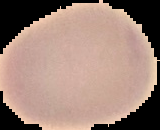

malaria status = uninfected
image type = cell region segmented out of the field of view; surrounding area masked to black
image size = 160×130 pixels
preparation = thin blood smear